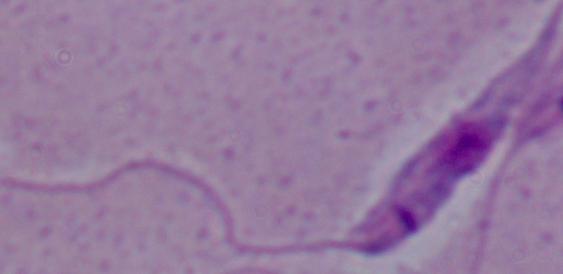
Captured at 1000x magnification. Photomicrograph. A Leishmania parasite is seen.